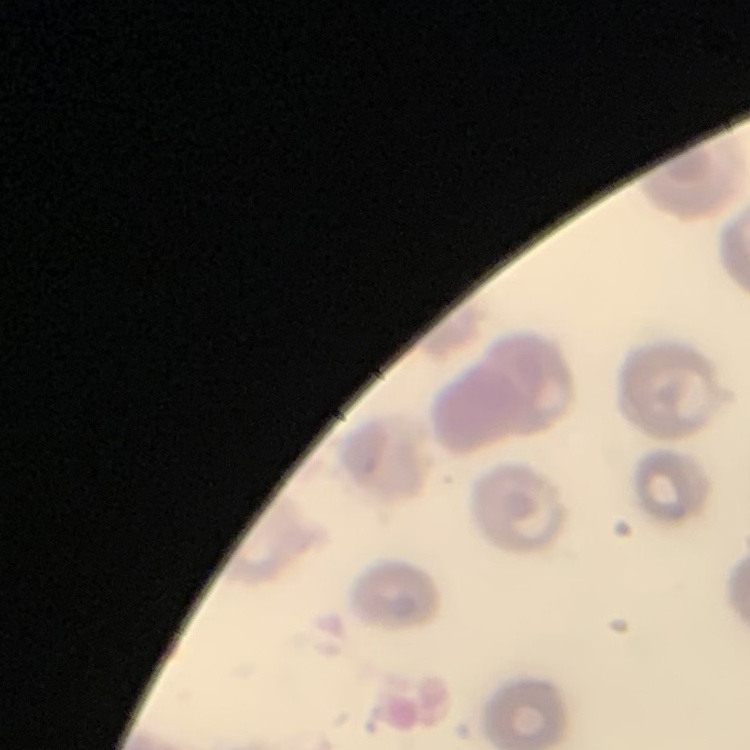
Summary:
  - Erythrocyte morphology: no rouleaux formation
  - Stain: Field's or Giemsa
  - Preparation: thin peripheral smear
  - Image type: one tile cut from a larger photomicrograph